Describe the morphology of the erythrocytes.
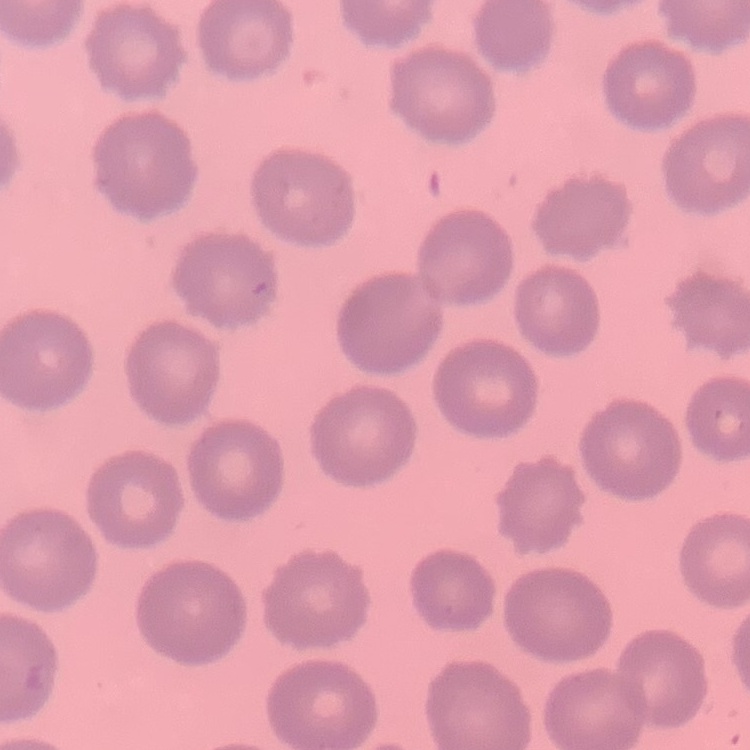

No rouleaux formation.

Thin blood film. One tile cut from a larger photomicrograph. Stained with either Field's or Giemsa.